Assess this cell for malaria.
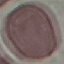

It is uninfected.

{
  "image_type": "cell patch, automatically extracted from a larger field of view and resized to 64 × 64 pixels",
  "preparation": "thin blood film",
  "capture": "smartphone through the microscope eyepiece",
  "stain": "Giemsa"
}